Locate Plasmodium parasites and leukocytes.
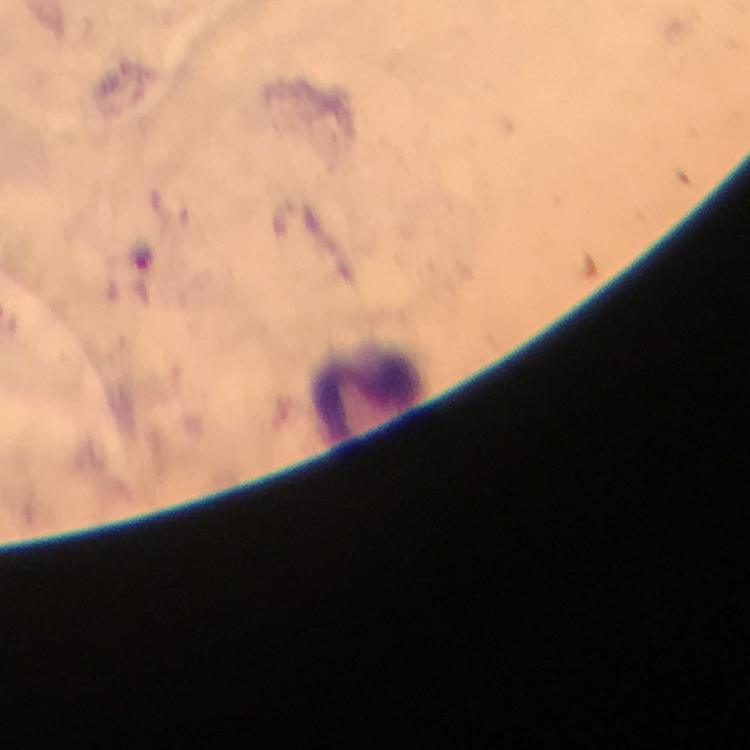

Approximate centers as [x, y] in pixels.
Plasmodium parasites: [141, 255].
Leukocytes: [366, 386].

stain = Giemsa
image size = 750×750 pixels
magnification = 100x
context = from a malaria diagnostic workup
immersion oil = applied
preparation = thick blood film
capture = smartphone mounted on the microscope
cropped from = one field of view